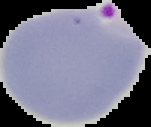
image_size: 151×127 pixels
preparation: thin blood smear
malaria_status: parasitized
image_type: cell region segmented out of the field of view; surrounding area masked to black